Comment on the morphology of the red blood cells.
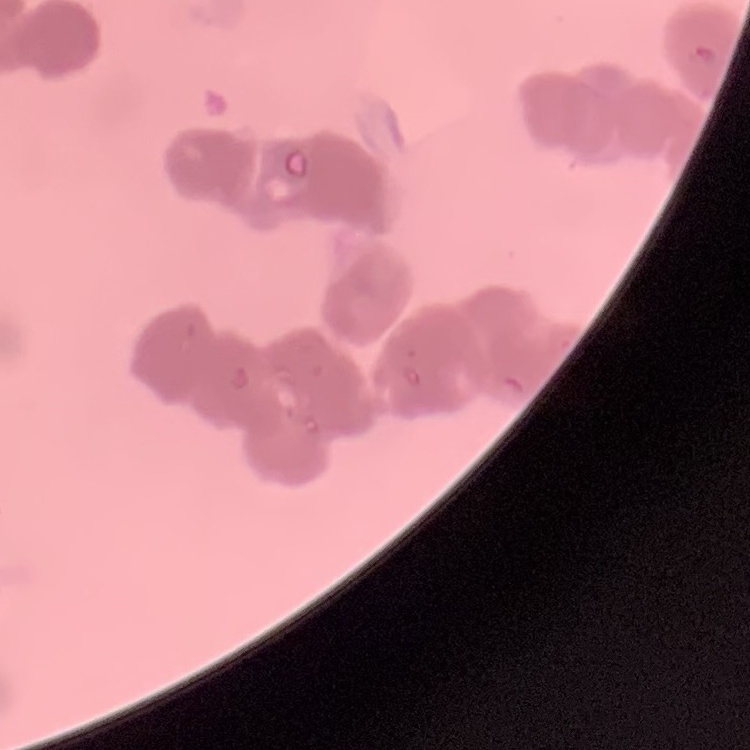
Rouleaux formation.

Field's or Giemsa stain. One tile cut from a larger photomicrograph. Thin blood smear.